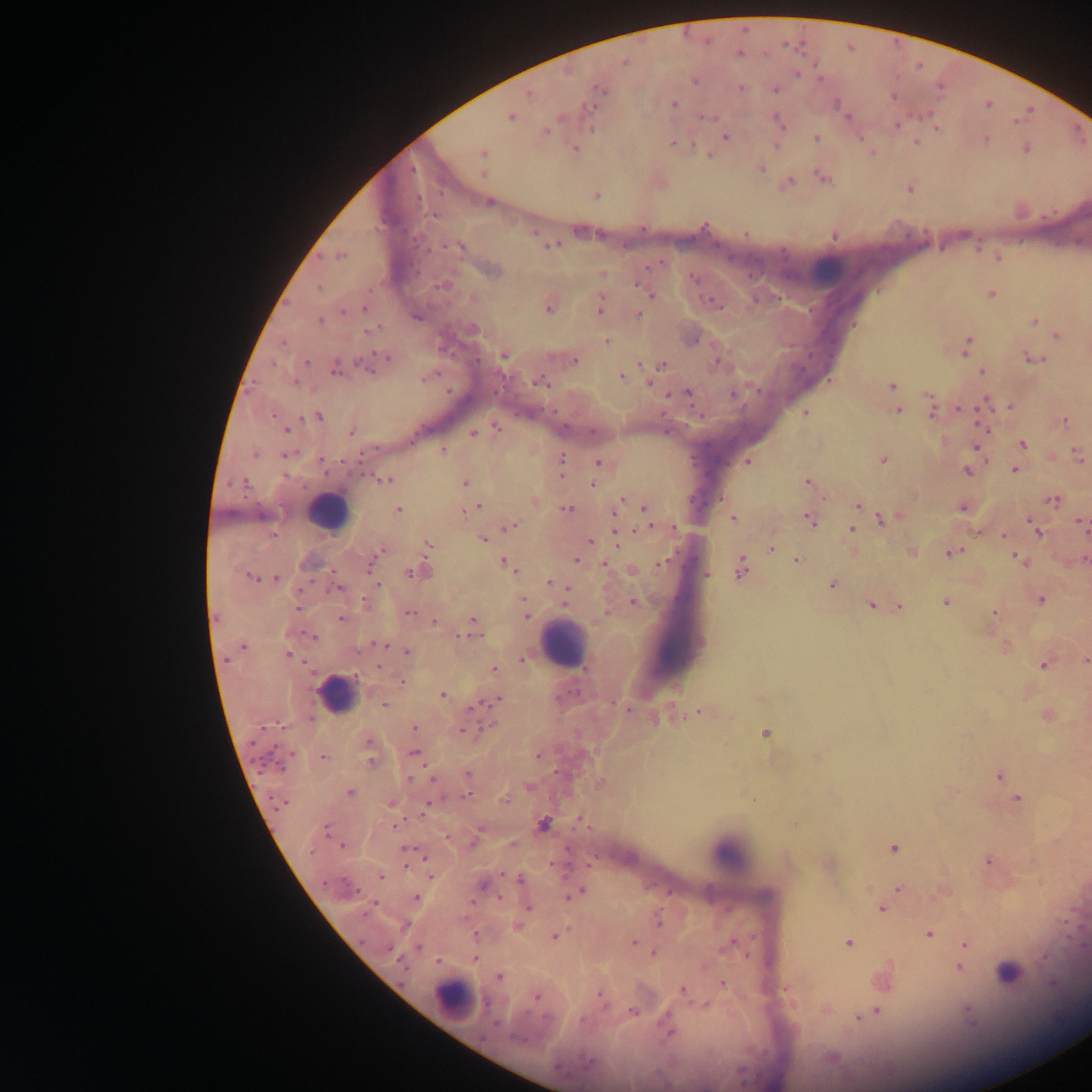
Approximate centers as (x, y) in pixels.
Summary:
  - Leukocyte locations: (826, 271), (327, 511), (563, 645), (336, 695), (728, 852), (1011, 963), (454, 1000)
  - Malaria parasite locations: (739, 53), (624, 62), (739, 87), (599, 89), (774, 89), (528, 93), (672, 104), (843, 113), (509, 116), (703, 116), (777, 119), (896, 126), (936, 127), (546, 131), (725, 136), (815, 138), (674, 142), (915, 142), (776, 143), (574, 147), (1026, 148), (483, 153), (760, 167), (823, 177), (786, 182), (909, 187), (595, 194), (488, 201), (834, 235), (550, 244), (458, 245), (340, 254), (997, 257), (490, 270), (694, 279), (641, 286), (648, 291), (990, 293), (713, 301), (549, 304), (600, 306), (365, 308), (638, 314), (320, 320), (1034, 322), (472, 329), (1057, 336), (692, 338), (606, 341), (966, 345), (504, 355), (383, 358), (1031, 358), (573, 360), (305, 362), (368, 363), (660, 365), (334, 367), (982, 371), (426, 376), (621, 376), (539, 381), (650, 382), (891, 385), (688, 393), (985, 403), (931, 406), (1010, 406), (958, 408), (897, 410), (805, 413), (318, 416), (1063, 420), (496, 428), (286, 429), (351, 431), (473, 432), (1022, 443), (979, 445), (443, 450), (255, 453), (286, 454), (1078, 455), (882, 459), (747, 460), (597, 461), (560, 467), (1014, 468), (968, 469), (385, 479), (807, 481), (464, 483), (593, 483), (533, 500), (1052, 500), (620, 502), (857, 505), (963, 506), (476, 507), (644, 507), (567, 508), (398, 510), (615, 510), (733, 517), (809, 518), (884, 518), (1081, 522), (510, 525), (650, 526), (852, 529), (1036, 530), (1004, 535), (616, 536), (483, 539), (589, 541), (429, 544), (771, 548), (378, 551), (912, 551), (952, 552), (375, 557), (1019, 559), (1084, 559), (576, 560), (796, 561), (506, 563), (661, 563), (371, 564), (604, 564), (741, 568), (632, 570), (418, 572), (705, 575), (251, 577), (273, 578), (551, 583), (831, 584), (1040, 599), (524, 601), (633, 602), (945, 602), (366, 604), (870, 605), (898, 605), (297, 608), (994, 611), (410, 612), (526, 614), (341, 618), (434, 622), (472, 626), (313, 637), (380, 645), (242, 646), (1005, 646), (407, 651), (288, 654), (524, 658), (1085, 660), (1045, 662), (494, 669), (402, 682), (442, 695), (498, 699), (384, 704), (698, 711), (1047, 715), (414, 727), (464, 729), (765, 733), (368, 746), (414, 752), (538, 755), (323, 757), (467, 774), (999, 775), (599, 782), (528, 787), (349, 792), (1017, 798), (391, 802), (581, 819), (543, 825), (512, 844), (342, 845), (893, 848), (407, 852), (987, 861), (827, 862), (431, 876), (381, 877), (520, 879), (483, 885), (899, 888), (577, 891), (941, 891), (416, 898), (527, 906), (882, 907), (659, 920), (517, 925), (929, 934), (475, 935), (554, 935), (633, 942), (731, 943), (849, 943), (965, 943), (653, 953), (474, 958), (438, 961), (958, 967), (499, 976), (883, 978), (722, 983), (786, 989), (682, 990), (600, 995), (536, 997), (706, 1005), (825, 1009), (967, 1010), (632, 1012), (875, 1012), (866, 1014), (858, 1017), (668, 1030)
  - Capture: mobile-phone photograph through a microscope
  - Preparation: thick blood film
  - Field of view: single
  - Country: Ghana
  - Image size: 1092×1092 pixels